Assess this cell for malaria.
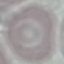

It is uninfected.

Summary:
  - Image type: automatically extracted cell patch, resized to 64 × 64 pixels
  - Stain: Giemsa
  - Preparation: thin blood film
  - Capture: smartphone through the microscope eyepiece